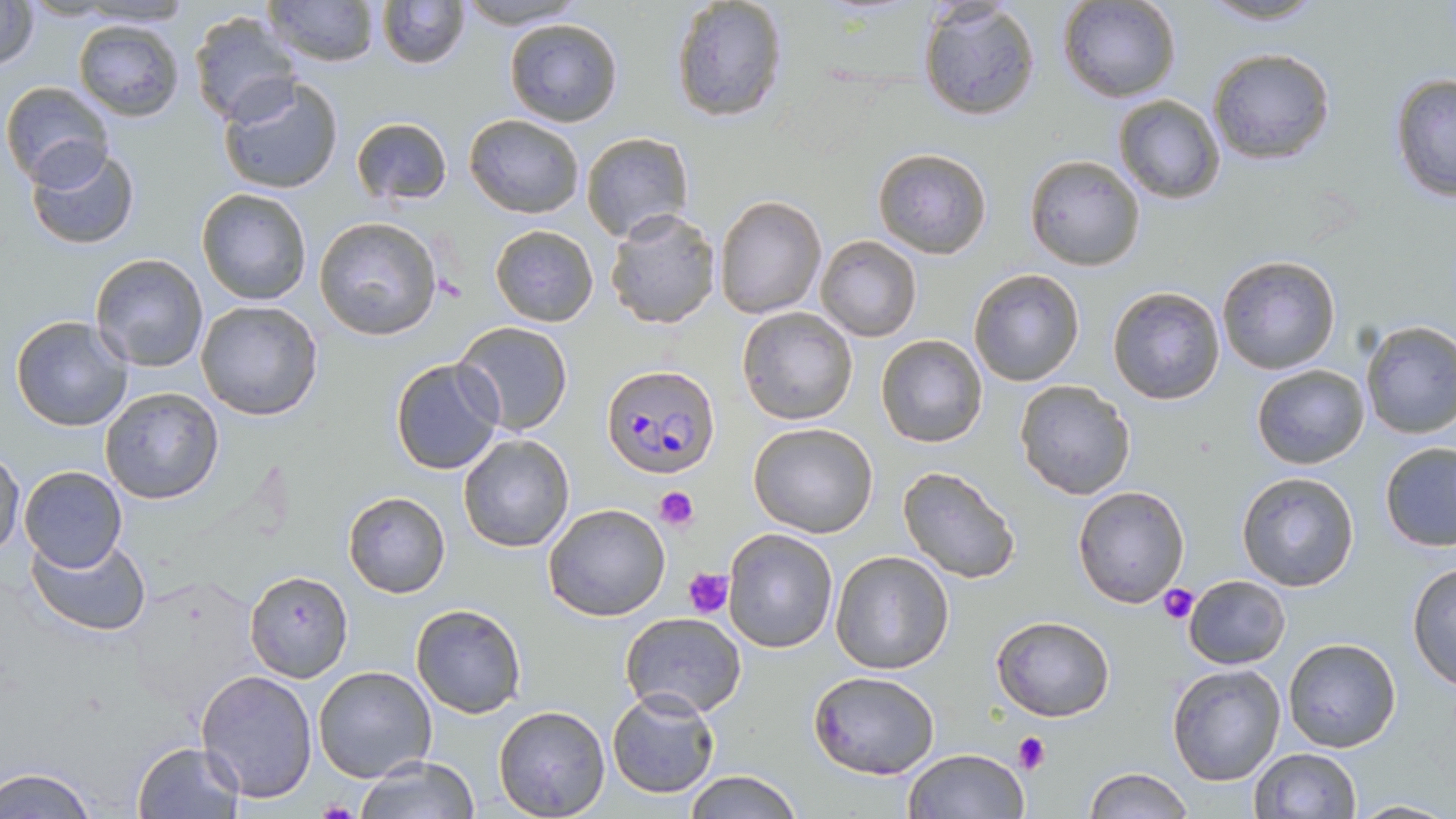 Approximate bounding boxes as (x1,y1)-(x2,y2) corner pairs in pixels. Uninfected red blood cell locations: (0,0)-(41,70), (265,0)-(380,67), (376,0)-(469,69), (455,0)-(588,29), (668,0)-(789,123), (1057,0)-(1182,104), (1198,0)-(1331,26), (73,1)-(196,28), (917,4)-(1041,120), (189,10)-(304,125), (503,18)-(624,128), (72,19)-(187,121), (1206,47)-(1336,166), (1387,72)-(1455,202), (218,76)-(345,194), (1,80)-(114,185), (1113,94)-(1226,204), (463,113)-(584,219), (349,115)-(453,206), (580,132)-(695,241), (23,143)-(142,253), (872,147)-(992,260), (1024,154)-(1147,272), (195,187)-(312,306), (715,196)-(826,318), (605,208)-(720,329), (313,215)-(441,340), (489,224)-(599,328), (815,235)-(923,341), (89,253)-(209,373), (1215,254)-(1341,375), (969,268)-(1084,387), (1105,286)-(1226,405), (195,300)-(324,421), (736,307)-(858,426), (9,314)-(133,430), (1359,320)-(1456,439), (452,321)-(574,436), (875,334)-(989,449), (389,357)-(504,475), (1250,364)-(1370,470), (1014,379)-(1138,499), (100,387)-(224,504), (747,421)-(878,537), (457,433)-(575,553), (1378,440)-(1456,551), (0,449)-(26,557), (18,465)-(129,569), (895,466)-(1022,584), (1235,471)-(1361,593), (1072,483)-(1190,608), (342,491)-(451,598), (542,503)-(672,621), (723,529)-(838,652), (26,534)-(154,638), (831,550)-(954,675), (1406,560)-(1456,692), (244,570)-(350,681), (1182,574)-(1290,669), (123,576)-(265,721), (409,602)-(526,718), (620,612)-(746,718), (990,613)-(1116,721), (1281,638)-(1401,754), (1167,664)-(1287,785), (312,666)-(436,783), (196,669)-(318,803), (809,669)-(940,780), (607,688)-(719,799), (494,705)-(611,817), (130,740)-(246,818), (1249,747)-(1362,819), (902,748)-(1028,819), (353,755)-(478,818), (0,765)-(98,819), (1081,767)-(1194,819), (683,770)-(802,819), (1349,797)-(1455,816). Plasmodium falciparum-infected red blood cell locations: (602,363)-(722,479). Platelet locations: (654,488)-(698,529), (683,566)-(736,617), (1158,584)-(1200,624), (1015,733)-(1050,772), (318,800)-(361,819). Slide-level diagnosis: Plasmodium falciparum. Optical microscopy. One field of a larger specimen. Image is 1456×819 pixels. 1000x magnification. Thin blood smear. May-Grünwald-Giemsa stain.